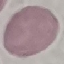

Summary:
  - Malaria status: uninfected
  - Stain: Giemsa
  - Image type: automatically extracted cell patch, resized to 64 × 64 pixels
  - Preparation: thin blood film
  - Capture: smartphone through the microscope eyepiece